Locate every Plasmodium ovale-infected red blood cell.
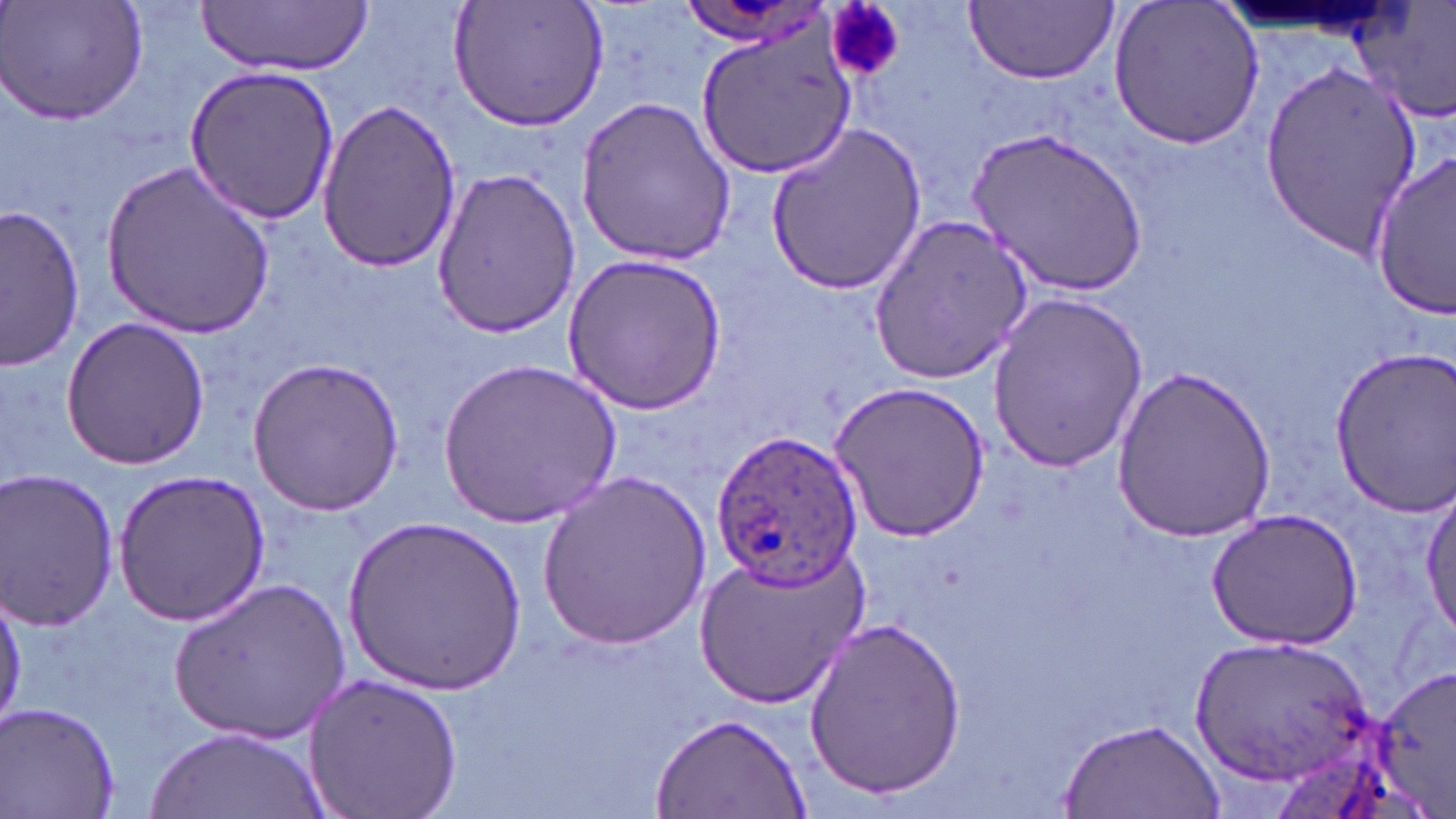

Approximate bounding boxes as (x1,y1)-(x2,y2) corner pairs in pixels.
Plasmodium ovale-infected red blood cells: (708,431)-(864,590).

slide-level diagnosis = Plasmodium ovale
platelet locations = approximate bounding boxes as (x1,y1)-(x2,y2) corner pairs in pixels: (835,0)-(908,87)
uninfected red blood cell locations = approximate bounding boxes as (x1,y1)-(x2,y2) corner pairs in pixels: (3,0)-(151,127), (199,0)-(374,75), (449,0)-(609,130), (963,1)-(1119,85), (1107,1)-(1266,152), (1355,2)-(1456,124), (695,18)-(858,177), (1259,59)-(1424,252), (183,63)-(340,226), (575,91)-(738,266), (317,100)-(462,270), (764,123)-(926,296), (972,124)-(1149,300), (1368,151)-(1456,320), (102,159)-(275,337), (429,165)-(581,340), (2,205)-(86,369), (867,213)-(1036,383), (558,251)-(731,417), (986,291)-(1147,472), (62,316)-(211,469), (1327,349)-(1456,514), (244,356)-(409,517), (441,359)-(621,527), (1110,368)-(1281,540), (830,379)-(991,544), (536,466)-(712,653), (0,469)-(121,630), (113,469)-(270,627), (1418,489)-(1455,644), (1204,508)-(1364,648), (345,514)-(525,698), (694,544)-(867,709), (171,576)-(351,743), (0,581)-(25,729), (802,615)-(965,800), (1195,633)-(1374,786), (1376,665)-(1456,813), (300,670)-(464,819), (2,703)-(120,818), (648,712)-(811,819), (1058,716)-(1225,819), (146,725)-(326,818)
image size = 1456×819 pixels
preparation = thin blood smear
modality = light microscopy
magnification = 1000x
stain = May-Grünwald-Giemsa
field of view = one of a larger specimen